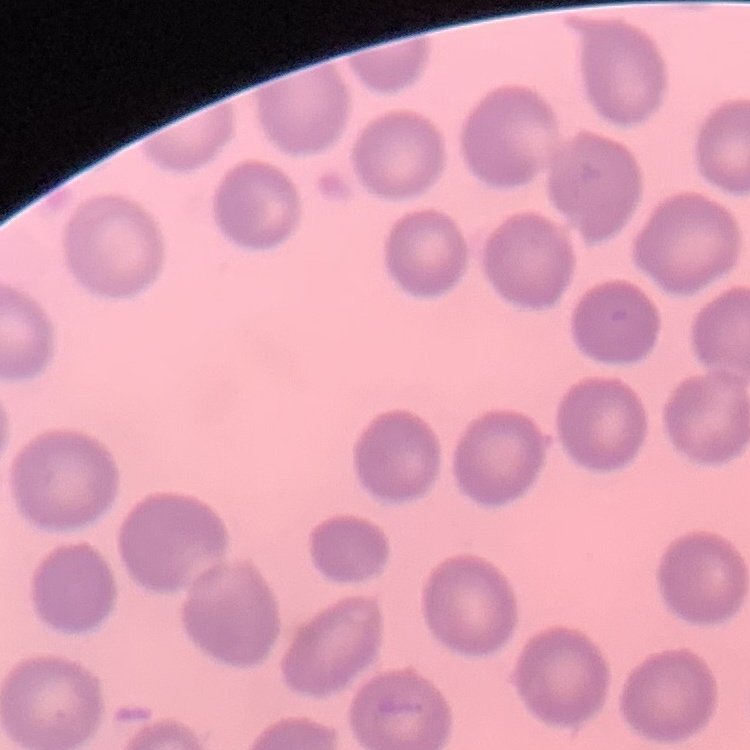
erythrocyte morphology = no rouleaux formation
image type = square crop of a larger photomicrograph
preparation = thin peripheral smear
stain = Field's or Giemsa